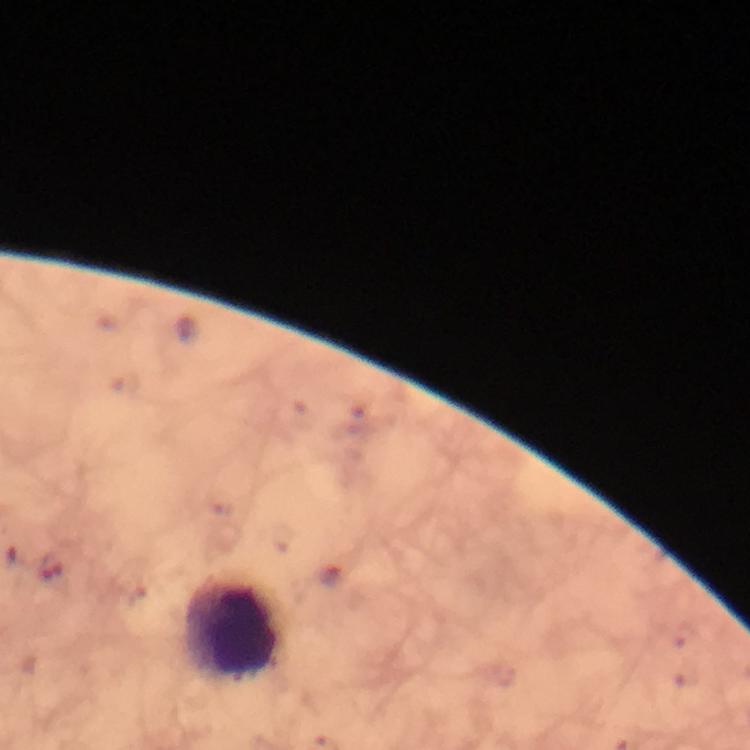 Approximate object centers, in pixels from the top-left corner. Malaria parasite locations: (x=49, y=567). Leukocyte locations: (x=235, y=629). Thick blood smear. Immersion oil applied. Image is 750×750 pixels. Giemsa stain. Cropped region of a single field of view. Photographed through the microscope with a smartphone camera. At 100x magnification. From a malaria diagnostic workup.